Name the parasite shown.
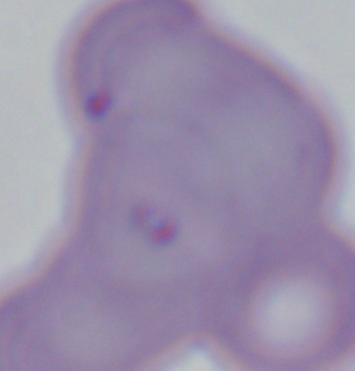

This is Babesia.

Summary:
  - Modality: micrograph
  - Magnification: 1000x